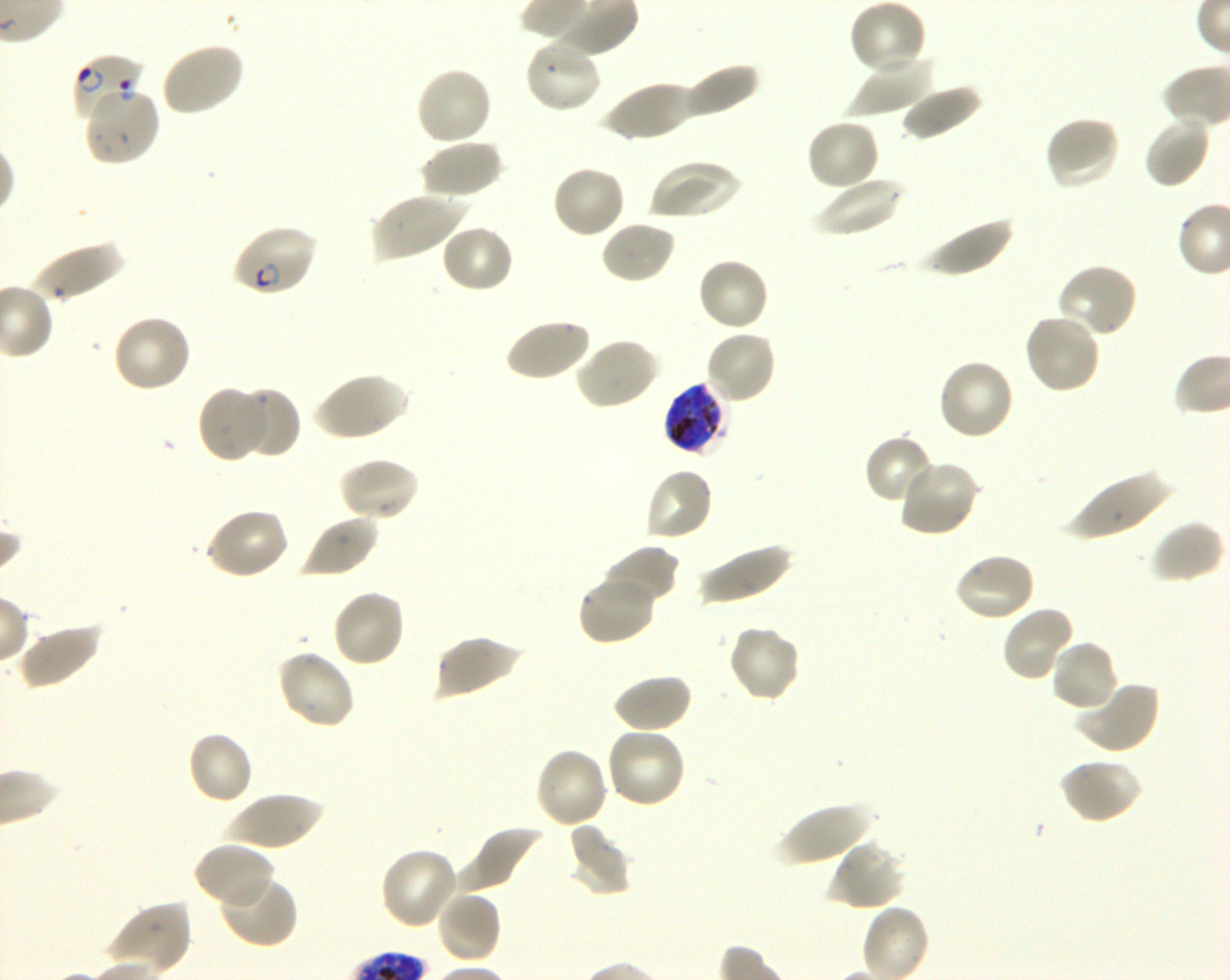
Approximate bounding boxes as (x1, y1, x2, y2) in pixels. Not every red blood cell is marked. A life-cycle stage — or a range of stages, where the recorded stages span more than one — follows each staged infected red blood cell.
Summary:
  - Locations of infected red blood cells: (71, 52, 145, 124) ring; (230, 223, 318, 297) early ring to early trophozoite; (662, 381, 728, 457) late trophozoite to late schizont
  - Locations of uninfected red blood cells: (849, 0, 927, 76), (524, 37, 602, 114), (159, 42, 244, 117), (850, 54, 933, 116), (680, 63, 761, 122), (415, 66, 493, 147), (599, 79, 694, 143), (901, 84, 984, 142), (83, 86, 161, 167), (1045, 114, 1121, 191), (1142, 114, 1211, 189), (804, 118, 881, 192), (420, 139, 503, 199), (648, 157, 741, 221), (551, 164, 627, 239), (810, 177, 907, 237), (370, 191, 465, 262), (917, 214, 1015, 279), (600, 220, 677, 285), (440, 224, 514, 295), (28, 241, 124, 303), (696, 257, 769, 333), (1055, 263, 1138, 338), (1023, 312, 1102, 396), (112, 314, 193, 394), (504, 317, 591, 383), (703, 329, 777, 406), (574, 337, 660, 411), (935, 357, 1015, 441), (313, 371, 407, 441), (197, 387, 267, 463), (236, 387, 300, 460), (863, 433, 935, 505), (337, 456, 419, 523), (896, 458, 980, 536), (643, 467, 715, 543), (1060, 472, 1173, 541), (204, 507, 290, 581), (300, 514, 379, 579), (1149, 521, 1225, 585), (697, 543, 794, 606), (601, 544, 679, 610), (952, 552, 1036, 624), (579, 574, 658, 645), (330, 588, 406, 668), (1001, 604, 1076, 683), (17, 621, 103, 689), (725, 624, 802, 703), (434, 634, 522, 700), (1049, 638, 1119, 713), (275, 649, 356, 731), (611, 672, 692, 734), (1073, 680, 1160, 755), (603, 726, 687, 810), (186, 730, 254, 805), (534, 747, 610, 830), (1059, 758, 1142, 825), (227, 792, 324, 850), (773, 801, 874, 866), (566, 822, 632, 897), (454, 826, 544, 896), (830, 838, 907, 911), (193, 842, 276, 912), (379, 845, 459, 929), (219, 871, 299, 947), (434, 890, 503, 964), (107, 900, 193, 976)
  - Field of view: one from this slide
  - Image size: 1230×980 pixels
  - Donor blood group: O+
  - Objective: 100x, oil immersion, numerical aperture 1.30
  - Preparation: thin blood film
  - Culture: shaking in-vitro P. falciparum strain 3D7
  - Stain: Giemsa